Report the malaria status of this cell.
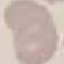

It is uninfected.

Cell patch, automatically extracted from a larger field of view and resized to 64 × 64 pixels. Thin blood smear. Photographed with a smartphone camera at the microscope eyepiece. Giemsa-stained preparation.